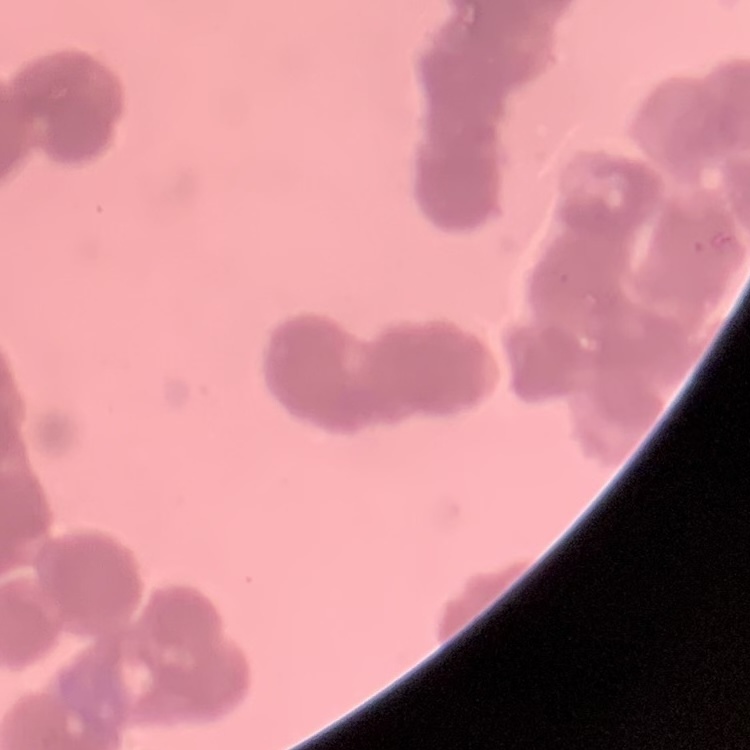
Summary:
  - Erythrocyte morphology: rouleaux formation
  - Stain: Field's or Giemsa
  - Image type: square crop of a larger photomicrograph
  - Preparation: thin peripheral smear